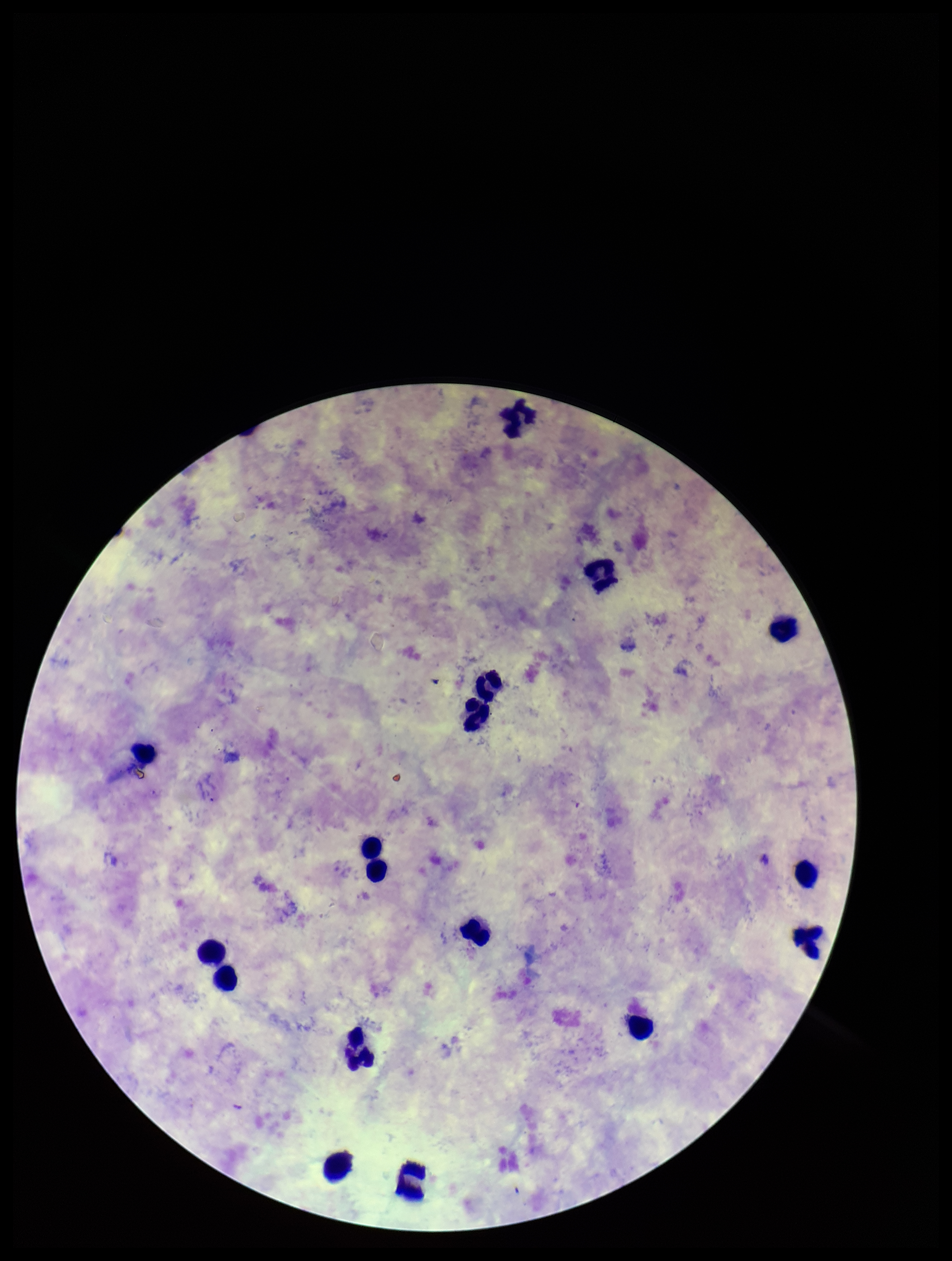

Giemsa stain. Preparation: thick smear. Species reported for this patient: Plasmodium vivax. Leukocyte count: 15. Parasite count: 0. Single field of view. Photographed through the microscope eyepiece with a smartphone camera. Patient malaria status: positive. Image is 952×1261 pixels. Plasmodium parasites: none seen.